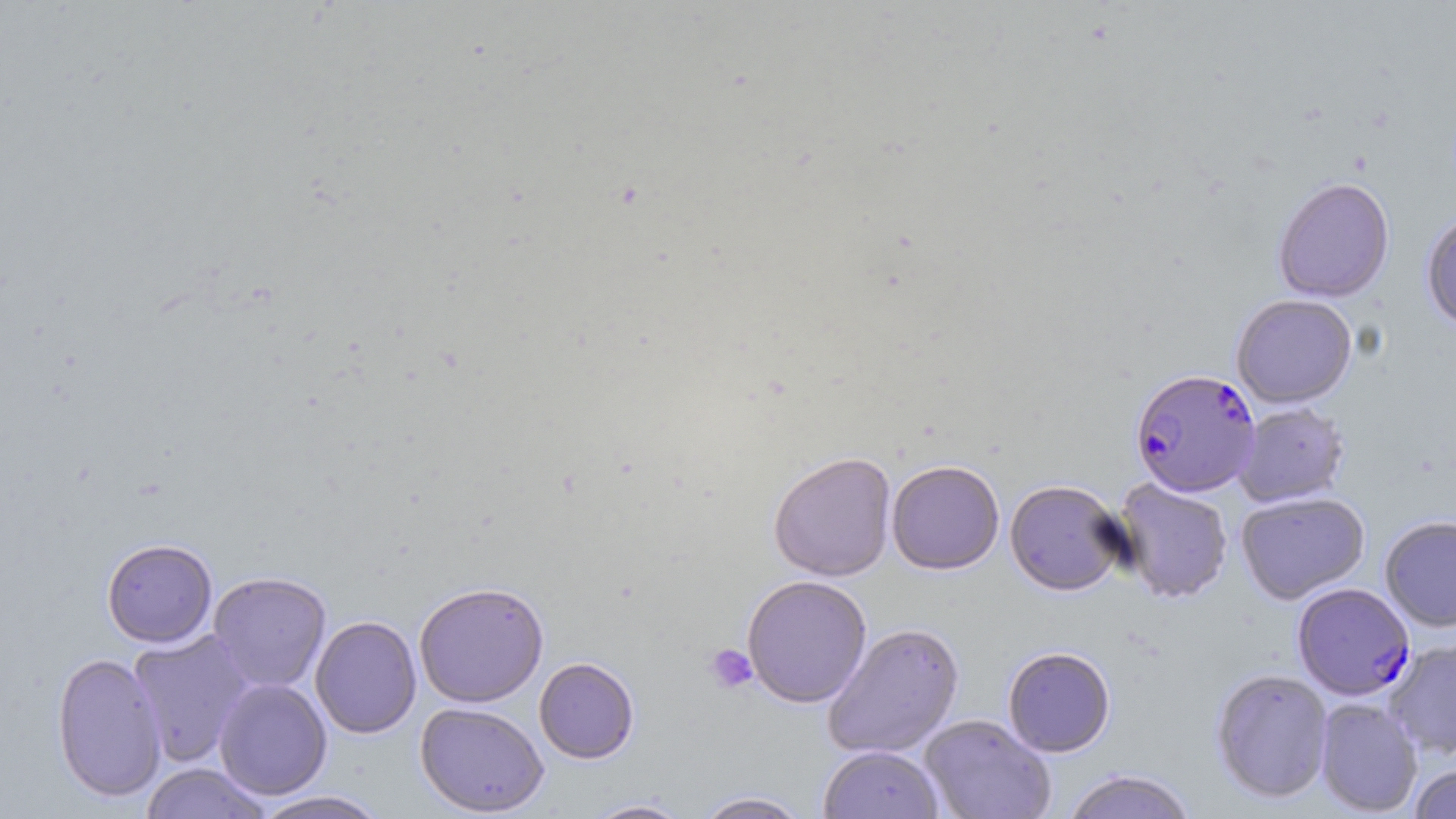 Approximate bounding boxes as (x1,y1)-(x2,y2) corner pairs in pixels. Plasmodium falciparum-infected red blood cell locations: (1130,369)-(1260,498), (1292,583)-(1415,701). Uninfected red blood cell locations: (1272,179)-(1395,304), (1421,212)-(1456,333), (1231,295)-(1357,409), (1233,403)-(1350,508), (768,450)-(897,582), (886,459)-(1004,575), (1113,478)-(1233,605), (1004,480)-(1128,597), (1235,492)-(1370,605), (1379,516)-(1456,632), (101,538)-(218,647), (207,571)-(331,693), (741,575)-(872,708), (413,581)-(549,707), (310,615)-(422,738), (822,621)-(965,760), (128,631)-(254,767), (1384,638)-(1456,758), (1002,646)-(1116,758), (51,651)-(167,802), (534,657)-(640,763), (1209,668)-(1333,804), (214,678)-(332,800), (1314,697)-(1423,816), (415,701)-(549,816), (919,714)-(1056,819), (818,745)-(944,819), (139,762)-(271,818), (1408,763)-(1456,819), (1060,770)-(1198,819), (250,790)-(392,819), (692,791)-(813,818), (580,797)-(694,818). Platelet locations: (704,643)-(757,694). Slide-level diagnosis: Plasmodium falciparum. Single field of view. Thin blood smear. Image is 1456×819 pixels. Captured at 1000x magnification. Optical microscopy. May-Grünwald-Giemsa stain.